Comment on the morphology of the erythrocytes.
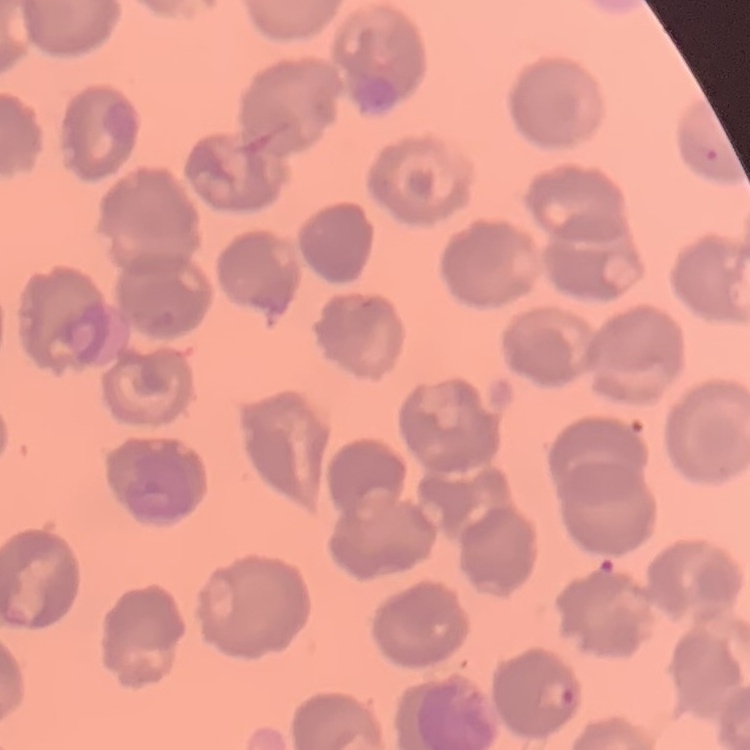

No rouleaux formation.

Stained with either Field's or Giemsa. Thin blood film. One tile cut from a larger photomicrograph.